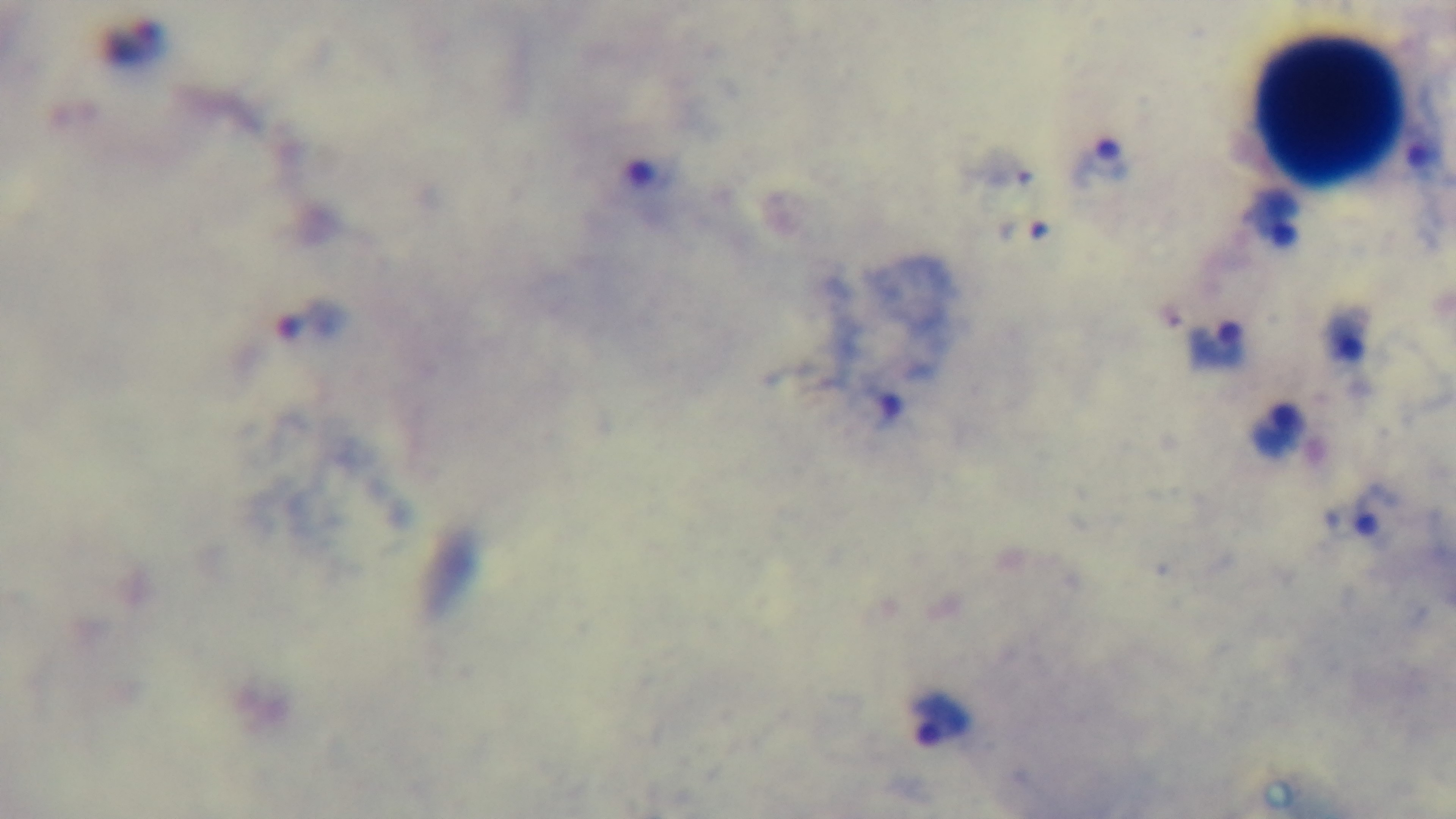

Summary:
  - Stain: Giemsa
  - Field of view: one from the slide
  - Malaria status: positive
  - Preparation: thick blood film
  - Objective: 100x oil immersion
  - Capture: mounted 4K digital camera
  - Modality: light microscopy